Outline each blood parasite and name the species.
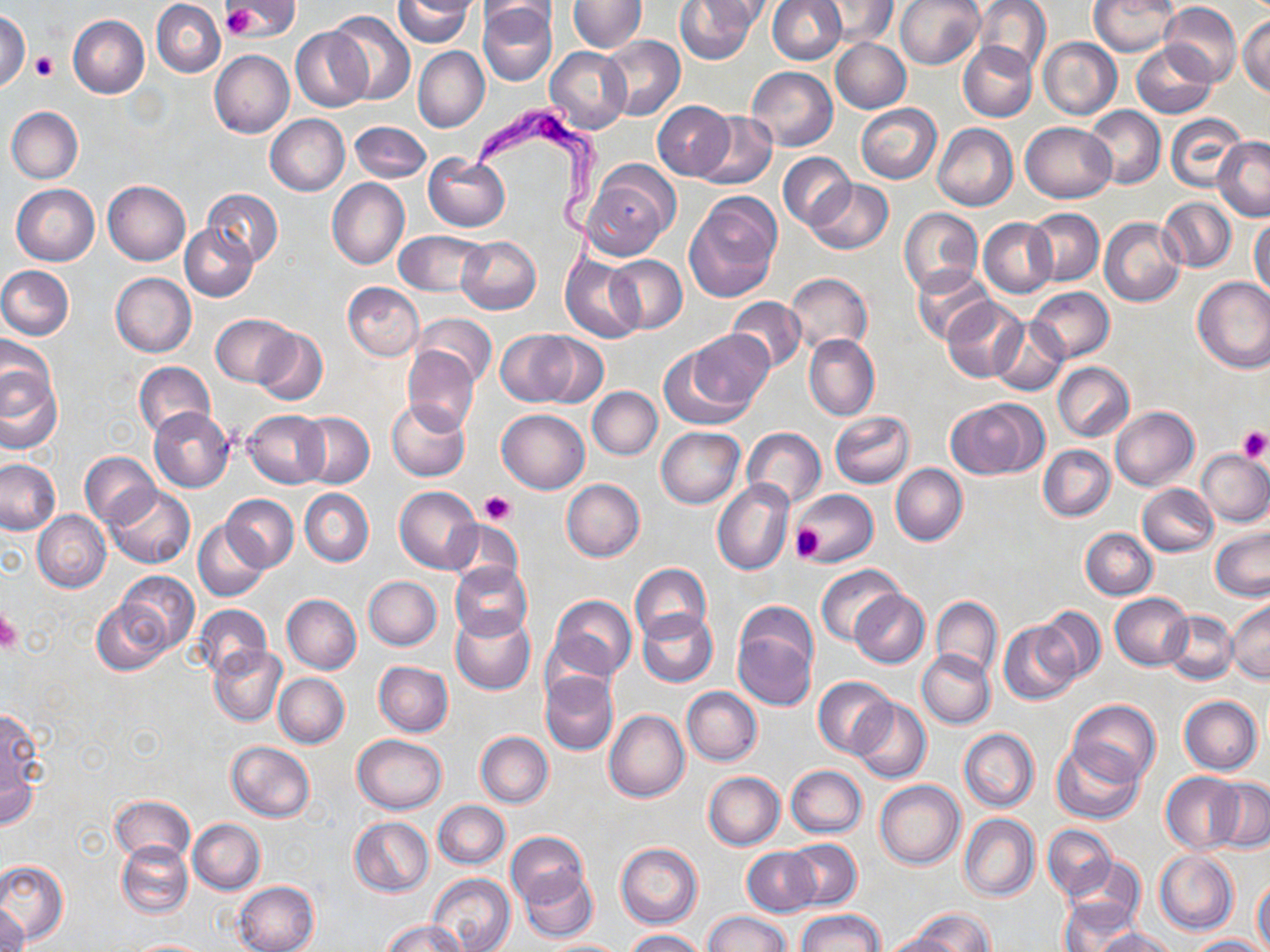
Approximate bounding boxes as named x1/y1/x2/y2 corners in pixels.
Trypanosoma brucei: (x1=472, y1=102, x2=604, y2=276).
No Plasmodium falciparum, Plasmodium ovale, Plasmodium malariae, Plasmodium vivax, or Babesia divergens observed.

Summary:
  - Platelet locations: (x1=223, y1=6, x2=259, y2=38), (x1=30, y1=51, x2=58, y2=81), (x1=1235, y1=424, x2=1270, y2=462), (x1=480, y1=491, x2=515, y2=526), (x1=790, y1=524, x2=826, y2=563), (x1=0, y1=608, x2=21, y2=654)
  - Uninfected red blood cell locations: (x1=225, y1=0, x2=295, y2=38), (x1=394, y1=0, x2=477, y2=48), (x1=675, y1=0, x2=759, y2=65), (x1=767, y1=0, x2=845, y2=64), (x1=895, y1=0, x2=985, y2=70), (x1=973, y1=0, x2=1051, y2=75), (x1=1089, y1=0, x2=1178, y2=56), (x1=152, y1=1, x2=225, y2=77), (x1=478, y1=1, x2=559, y2=29), (x1=568, y1=1, x2=646, y2=52), (x1=696, y1=1, x2=775, y2=31), (x1=813, y1=1, x2=899, y2=46), (x1=478, y1=2, x2=557, y2=87), (x1=1159, y1=3, x2=1242, y2=86), (x1=328, y1=10, x2=415, y2=104), (x1=0, y1=11, x2=30, y2=92), (x1=1238, y1=14, x2=1270, y2=97), (x1=67, y1=16, x2=149, y2=98), (x1=292, y1=26, x2=372, y2=112), (x1=599, y1=35, x2=685, y2=121), (x1=1038, y1=37, x2=1121, y2=119), (x1=830, y1=38, x2=911, y2=113), (x1=958, y1=42, x2=1036, y2=122), (x1=1131, y1=43, x2=1216, y2=118), (x1=546, y1=46, x2=632, y2=135), (x1=414, y1=47, x2=489, y2=132), (x1=210, y1=50, x2=293, y2=138), (x1=747, y1=66, x2=837, y2=151), (x1=653, y1=100, x2=733, y2=181), (x1=855, y1=104, x2=942, y2=183), (x1=1084, y1=105, x2=1164, y2=189), (x1=5, y1=107, x2=83, y2=183), (x1=1166, y1=112, x2=1248, y2=193), (x1=695, y1=113, x2=777, y2=189), (x1=264, y1=114, x2=350, y2=196), (x1=1020, y1=120, x2=1116, y2=202), (x1=349, y1=121, x2=432, y2=183), (x1=932, y1=123, x2=1017, y2=211), (x1=1213, y1=136, x2=1270, y2=221), (x1=423, y1=153, x2=510, y2=231), (x1=778, y1=153, x2=855, y2=229), (x1=581, y1=162, x2=679, y2=260), (x1=327, y1=178, x2=409, y2=269), (x1=806, y1=179, x2=894, y2=255), (x1=103, y1=180, x2=191, y2=265), (x1=12, y1=184, x2=100, y2=265), (x1=202, y1=188, x2=283, y2=265), (x1=685, y1=192, x2=782, y2=301), (x1=1159, y1=197, x2=1236, y2=273), (x1=898, y1=207, x2=983, y2=295), (x1=1027, y1=209, x2=1103, y2=286), (x1=1249, y1=216, x2=1270, y2=297), (x1=979, y1=217, x2=1057, y2=297), (x1=1099, y1=217, x2=1186, y2=307), (x1=180, y1=224, x2=258, y2=301), (x1=393, y1=231, x2=489, y2=296), (x1=455, y1=237, x2=541, y2=314), (x1=561, y1=253, x2=644, y2=343), (x1=604, y1=255, x2=687, y2=334), (x1=911, y1=264, x2=996, y2=346), (x1=0, y1=265, x2=74, y2=340), (x1=111, y1=273, x2=197, y2=357), (x1=785, y1=273, x2=872, y2=354), (x1=1192, y1=276, x2=1270, y2=373), (x1=343, y1=282, x2=424, y2=360), (x1=1028, y1=286, x2=1114, y2=361), (x1=728, y1=296, x2=805, y2=373), (x1=942, y1=296, x2=1029, y2=382), (x1=413, y1=313, x2=496, y2=388), (x1=211, y1=314, x2=293, y2=386), (x1=989, y1=317, x2=1069, y2=398), (x1=253, y1=327, x2=327, y2=406), (x1=687, y1=329, x2=773, y2=412), (x1=496, y1=331, x2=578, y2=406), (x1=531, y1=333, x2=608, y2=408), (x1=804, y1=333, x2=879, y2=422), (x1=0, y1=338, x2=55, y2=414), (x1=402, y1=345, x2=479, y2=437), (x1=657, y1=345, x2=751, y2=430), (x1=1, y1=356, x2=62, y2=455), (x1=135, y1=360, x2=216, y2=440), (x1=1052, y1=362, x2=1133, y2=440), (x1=587, y1=387, x2=662, y2=460), (x1=946, y1=398, x2=1045, y2=479), (x1=387, y1=399, x2=472, y2=482), (x1=1110, y1=405, x2=1199, y2=491), (x1=148, y1=407, x2=235, y2=492), (x1=497, y1=408, x2=589, y2=494), (x1=243, y1=409, x2=329, y2=488), (x1=828, y1=411, x2=914, y2=489), (x1=296, y1=412, x2=374, y2=487), (x1=656, y1=426, x2=746, y2=509), (x1=742, y1=427, x2=825, y2=510), (x1=1038, y1=445, x2=1115, y2=521), (x1=1197, y1=450, x2=1270, y2=525), (x1=80, y1=452, x2=159, y2=527), (x1=0, y1=459, x2=61, y2=534), (x1=891, y1=464, x2=967, y2=545), (x1=562, y1=479, x2=645, y2=562), (x1=712, y1=480, x2=795, y2=576), (x1=1138, y1=484, x2=1217, y2=556), (x1=105, y1=485, x2=195, y2=569), (x1=393, y1=485, x2=481, y2=573), (x1=791, y1=488, x2=878, y2=567), (x1=301, y1=489, x2=373, y2=565), (x1=222, y1=495, x2=298, y2=570), (x1=33, y1=510, x2=111, y2=592), (x1=443, y1=519, x2=522, y2=589), (x1=194, y1=521, x2=269, y2=601), (x1=1209, y1=526, x2=1269, y2=601), (x1=1080, y1=528, x2=1157, y2=599), (x1=449, y1=562, x2=532, y2=641), (x1=630, y1=563, x2=712, y2=642), (x1=816, y1=565, x2=904, y2=645), (x1=115, y1=571, x2=199, y2=653), (x1=363, y1=576, x2=442, y2=650), (x1=849, y1=590, x2=930, y2=668), (x1=283, y1=593, x2=361, y2=674), (x1=1110, y1=593, x2=1193, y2=669), (x1=549, y1=595, x2=636, y2=681), (x1=931, y1=595, x2=1003, y2=679), (x1=92, y1=597, x2=173, y2=675), (x1=1228, y1=598, x2=1270, y2=684), (x1=193, y1=604, x2=272, y2=680), (x1=1037, y1=605, x2=1105, y2=682), (x1=636, y1=609, x2=718, y2=687), (x1=1163, y1=611, x2=1238, y2=684), (x1=450, y1=612, x2=537, y2=694), (x1=732, y1=613, x2=817, y2=711), (x1=998, y1=620, x2=1080, y2=704), (x1=210, y1=646, x2=287, y2=725), (x1=918, y1=650, x2=995, y2=727), (x1=374, y1=660, x2=453, y2=736), (x1=540, y1=669, x2=619, y2=756), (x1=274, y1=674, x2=350, y2=747), (x1=814, y1=677, x2=896, y2=758), (x1=682, y1=687, x2=762, y2=765), (x1=1178, y1=696, x2=1261, y2=775), (x1=850, y1=698, x2=931, y2=783), (x1=1069, y1=699, x2=1160, y2=786), (x1=0, y1=703, x2=46, y2=823), (x1=604, y1=710, x2=688, y2=802), (x1=958, y1=728, x2=1038, y2=812), (x1=476, y1=731, x2=553, y2=807), (x1=353, y1=734, x2=447, y2=814), (x1=227, y1=741, x2=314, y2=822), (x1=1052, y1=742, x2=1146, y2=824), (x1=786, y1=765, x2=866, y2=838), (x1=704, y1=771, x2=784, y2=850), (x1=1161, y1=773, x2=1244, y2=854), (x1=1208, y1=779, x2=1269, y2=853), (x1=875, y1=781, x2=964, y2=868), (x1=110, y1=794, x2=195, y2=863), (x1=433, y1=801, x2=510, y2=869), (x1=959, y1=813, x2=1039, y2=901), (x1=349, y1=816, x2=433, y2=896), (x1=189, y1=819, x2=264, y2=894), (x1=1043, y1=824, x2=1116, y2=900), (x1=504, y1=832, x2=588, y2=909), (x1=784, y1=838, x2=861, y2=910), (x1=116, y1=840, x2=193, y2=918), (x1=616, y1=842, x2=703, y2=928), (x1=742, y1=847, x2=820, y2=918), (x1=1154, y1=850, x2=1238, y2=935), (x1=1063, y1=855, x2=1147, y2=928), (x1=0, y1=861, x2=67, y2=945), (x1=520, y1=869, x2=598, y2=942), (x1=428, y1=873, x2=515, y2=952), (x1=1253, y1=874, x2=1270, y2=950), (x1=232, y1=881, x2=319, y2=952), (x1=1059, y1=898, x2=1140, y2=952), (x1=1, y1=904, x2=28, y2=952), (x1=912, y1=907, x2=993, y2=952), (x1=796, y1=908, x2=884, y2=951), (x1=702, y1=909, x2=792, y2=952), (x1=383, y1=919, x2=467, y2=952), (x1=1095, y1=928, x2=1178, y2=952), (x1=625, y1=929, x2=703, y2=951), (x1=879, y1=931, x2=959, y2=952), (x1=1186, y1=934, x2=1266, y2=952), (x1=126, y1=939, x2=210, y2=951), (x1=541, y1=939, x2=627, y2=951)
  - Slide-level diagnosis: Trypanosoma brucei
  - Modality: optical microscopy
  - Magnification: 1000x
  - Preparation: thin blood smear
  - Stain: May-Grünwald-Giemsa
  - Image size: 1270×952 pixels
  - Field of view: one of a larger specimen